Point out each malaria parasite.
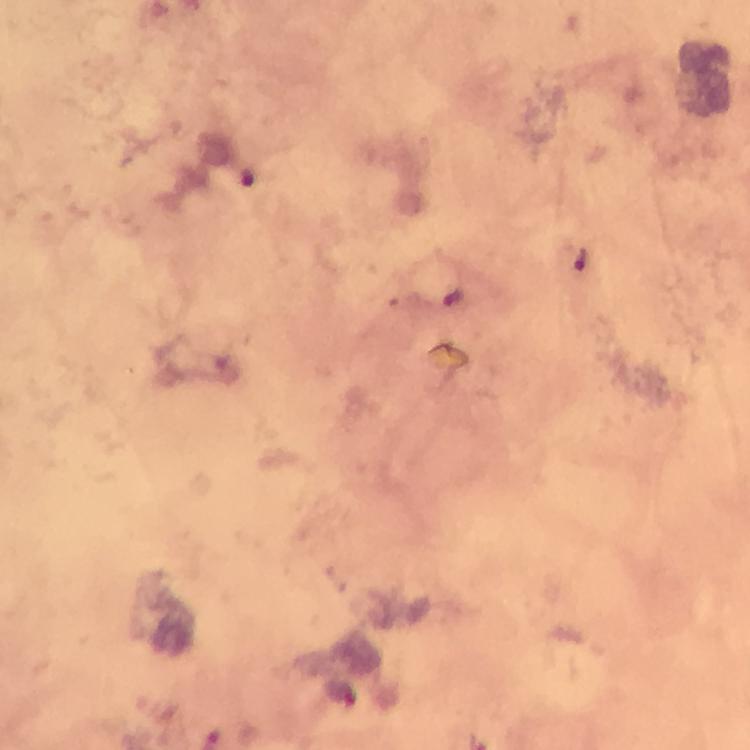
Approximate centers as (x, y) in pixels.
Malaria parasites: (581, 258).

cropped from = a single field of view
magnification = 100x
context = from a diagnostic examination for malaria
preparation = thick blood smear
capture = smartphone mounted on the microscope
image size = 750×750 pixels
immersion oil = used
stain = Giemsa